Name the blood parasite species.
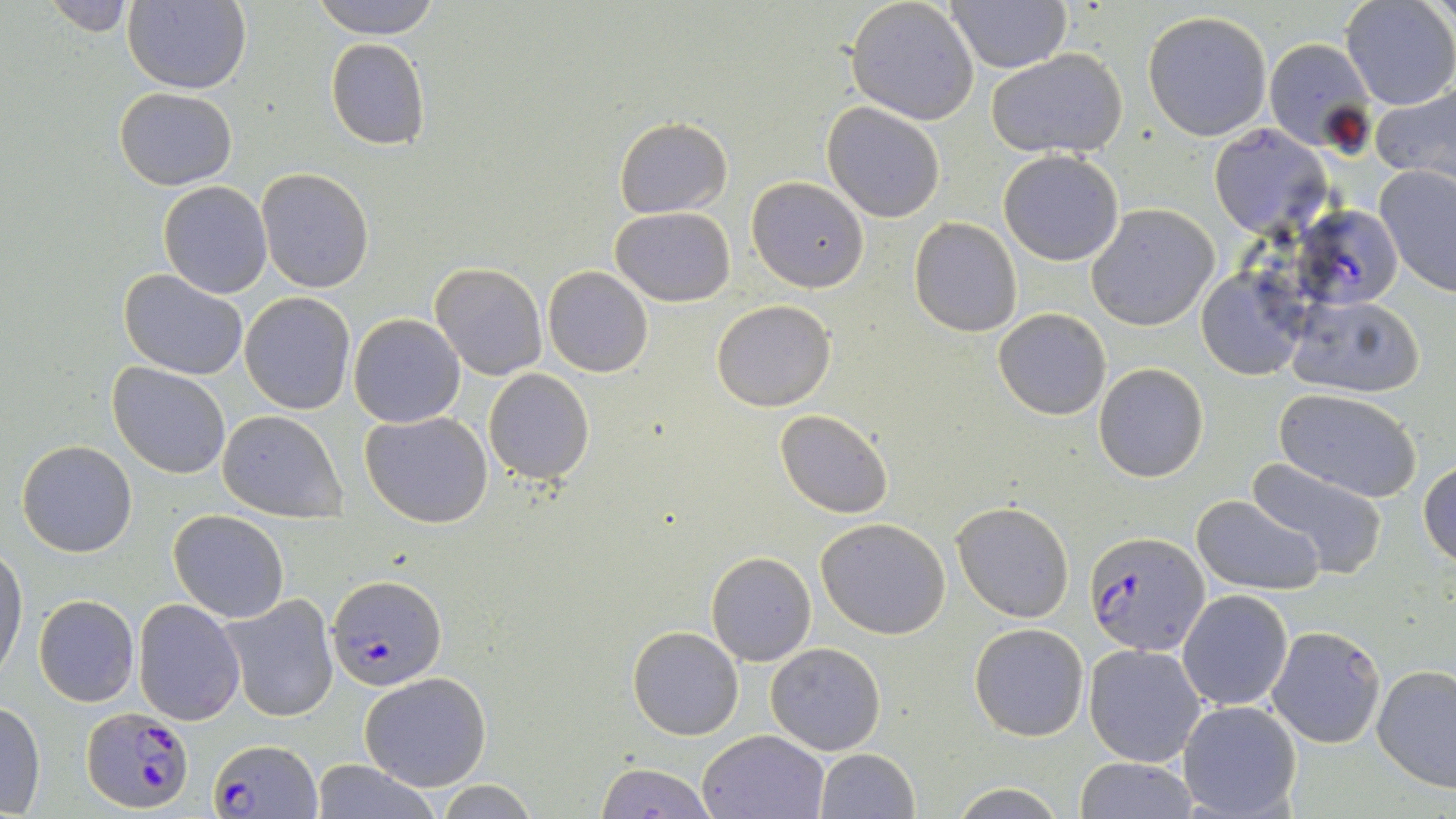
Plasmodium falciparum.

Approximate bounding boxes as [x1, y1, x2, y2] in pixels. Plasmodium falciparum-infected red blood cell locations: [1294, 209, 1402, 308], [1086, 531, 1209, 655], [327, 574, 448, 691], [83, 706, 194, 812], [211, 737, 321, 817]. Uninfected red blood cell locations: [37, 0, 143, 34], [312, 0, 439, 40], [845, 0, 980, 125], [1339, 0, 1455, 111], [122, 1, 252, 93], [948, 2, 1071, 73], [1142, 10, 1274, 142], [1263, 36, 1374, 152], [325, 38, 431, 151], [987, 47, 1127, 159], [1369, 79, 1456, 189], [115, 88, 238, 189], [823, 102, 944, 222], [613, 117, 734, 219], [1208, 123, 1333, 238], [998, 150, 1125, 266], [1376, 164, 1456, 296], [256, 167, 375, 295], [746, 176, 870, 292], [157, 182, 272, 299], [1087, 203, 1219, 331], [610, 206, 736, 307], [909, 217, 1023, 337], [430, 262, 548, 380], [542, 266, 653, 378], [119, 268, 249, 380], [1196, 268, 1307, 381], [240, 293, 355, 413], [1285, 294, 1427, 399], [711, 299, 836, 411], [993, 307, 1111, 421], [349, 314, 466, 427], [108, 363, 232, 479], [1094, 363, 1208, 483], [483, 367, 596, 484], [1275, 388, 1423, 503], [774, 409, 893, 519], [216, 410, 346, 523], [360, 411, 493, 529], [17, 440, 138, 558], [1244, 458, 1390, 580], [1419, 460, 1456, 566], [1191, 494, 1325, 597], [952, 500, 1075, 622], [168, 510, 289, 622], [815, 518, 951, 640], [0, 546, 27, 679], [706, 550, 816, 666], [1177, 590, 1292, 711], [33, 594, 140, 707], [222, 595, 339, 723], [134, 598, 246, 723], [969, 623, 1089, 740], [627, 626, 744, 741], [1267, 626, 1386, 748], [765, 641, 886, 755], [1084, 643, 1208, 767], [1373, 664, 1456, 791], [359, 673, 492, 791], [1177, 700, 1302, 818], [0, 701, 46, 816], [699, 729, 828, 818], [814, 749, 919, 819], [1072, 757, 1201, 817], [312, 760, 440, 818], [595, 764, 716, 818], [433, 780, 539, 818], [945, 784, 1071, 818]. Light microscopy. Image is 1456×819 pixels. Thin blood smear. Single field of view. May-Grünwald-Giemsa stain. Captured at 1000x magnification.